Outline Plasmodium falciparum parasites and classify them by life-cycle stage.
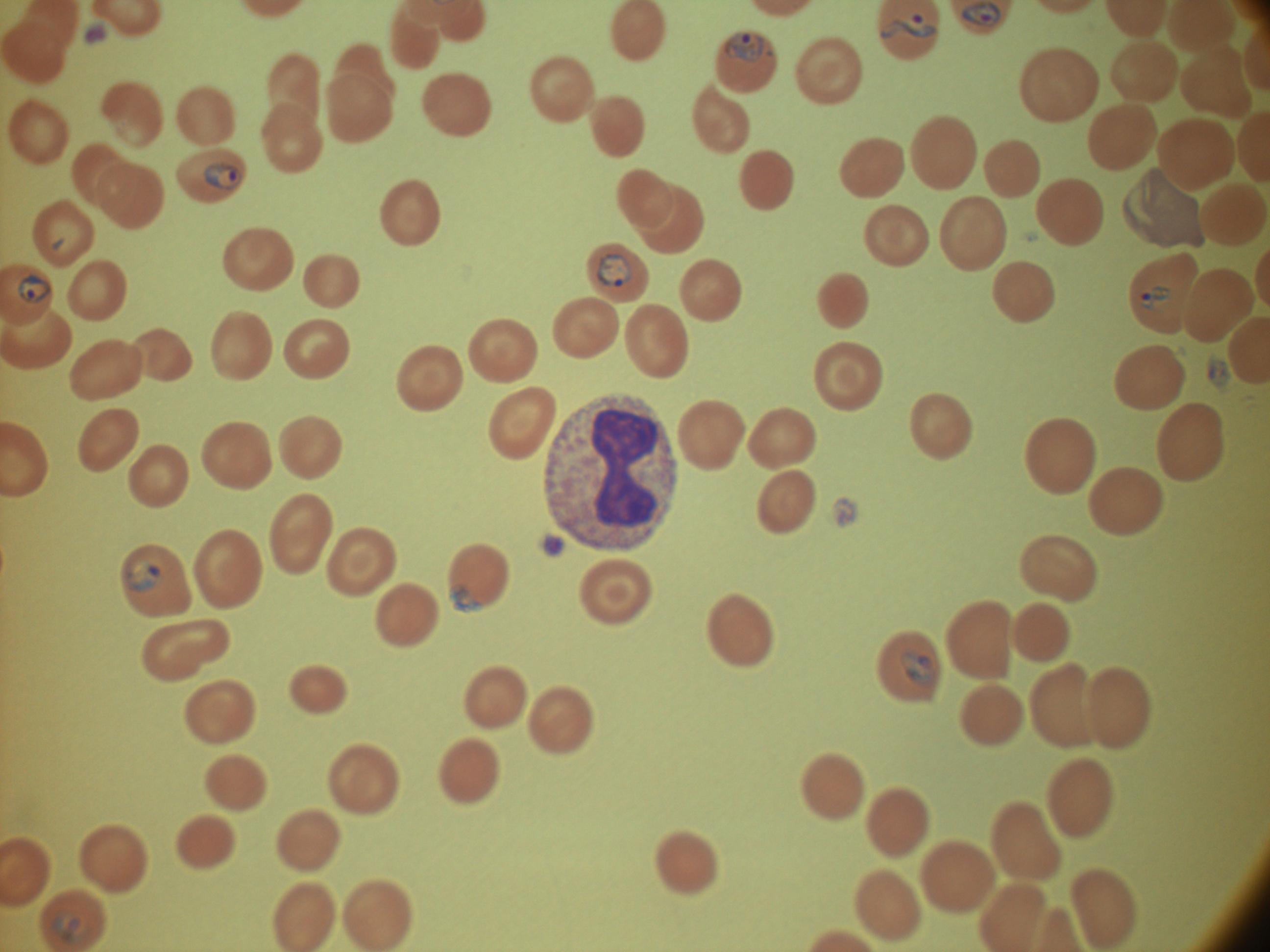
Approximate bounding boxes as (x1,y1)-(x2,y2) corner pairs in pixels, from the source annotation, which is not necessarily exhaustive.
Ring forms: (882,12)-(938,40), (726,31)-(765,64), (205,163)-(242,190), (596,253)-(632,288), (17,274)-(53,305), (1140,286)-(1170,309), (130,560)-(161,593), (449,584)-(484,614), (900,647)-(935,686), (51,911)-(88,944).

{
  "magnification": "100x",
  "microscope": "Leica DM2000 with built-in camera",
  "species": "Plasmodium falciparum",
  "stain": "Giemsa",
  "image_size": "1270×952 pixels",
  "preparation": "thin blood film",
  "field_of_view": "one from this slide"
}